Assess the morphology of the red blood cells.
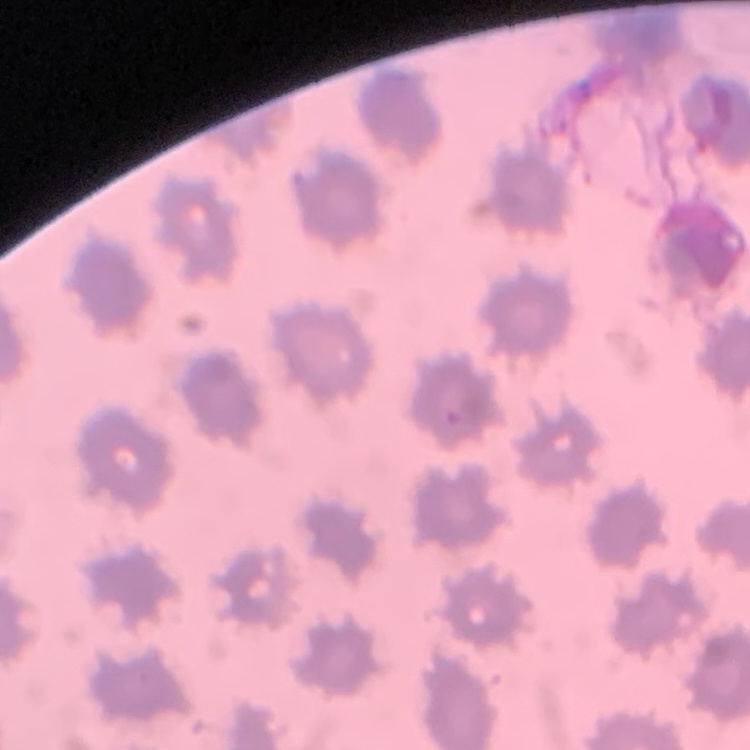

They show no rouleaux formation.

Stained with either Field's or Giemsa. Square crop of a larger photomicrograph. Thin peripheral smear.